Assess the morphology of the red blood cells.
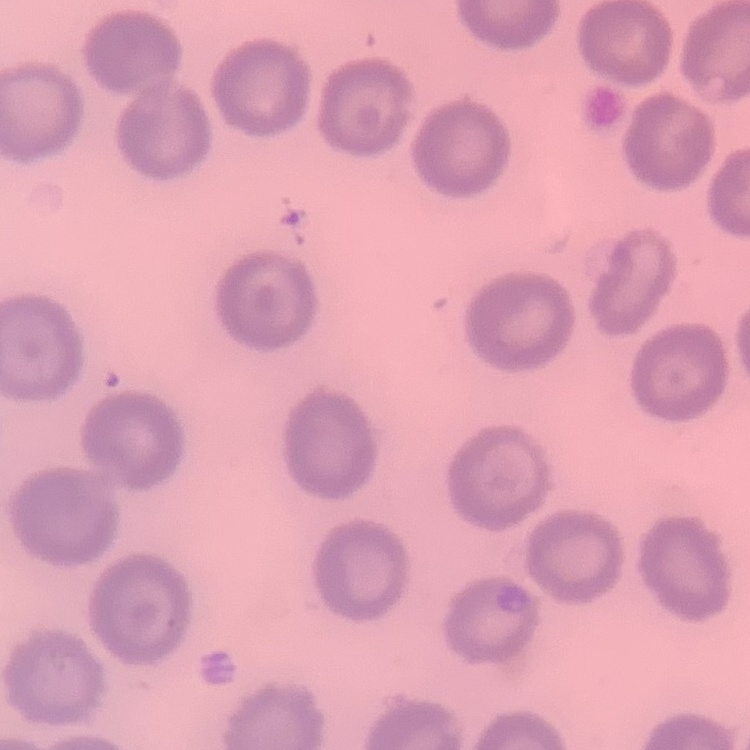

No rouleaux formation.

stain: Field's or Giemsa
image_type: square crop of a larger photomicrograph
preparation: thin blood smear